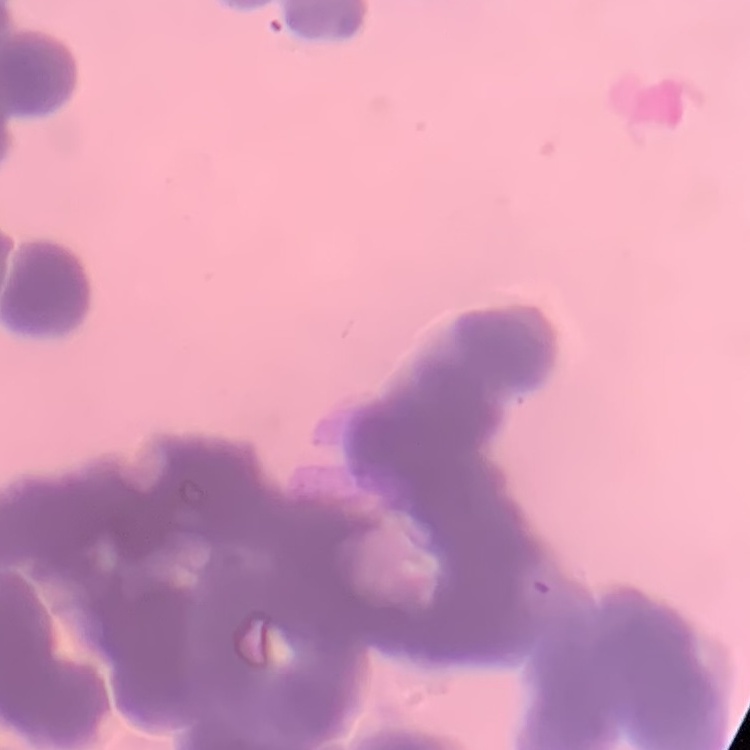 The erythrocytes show rouleaux formation. Thin blood film. One tile cut from a larger photomicrograph. Field's or Giemsa stain.